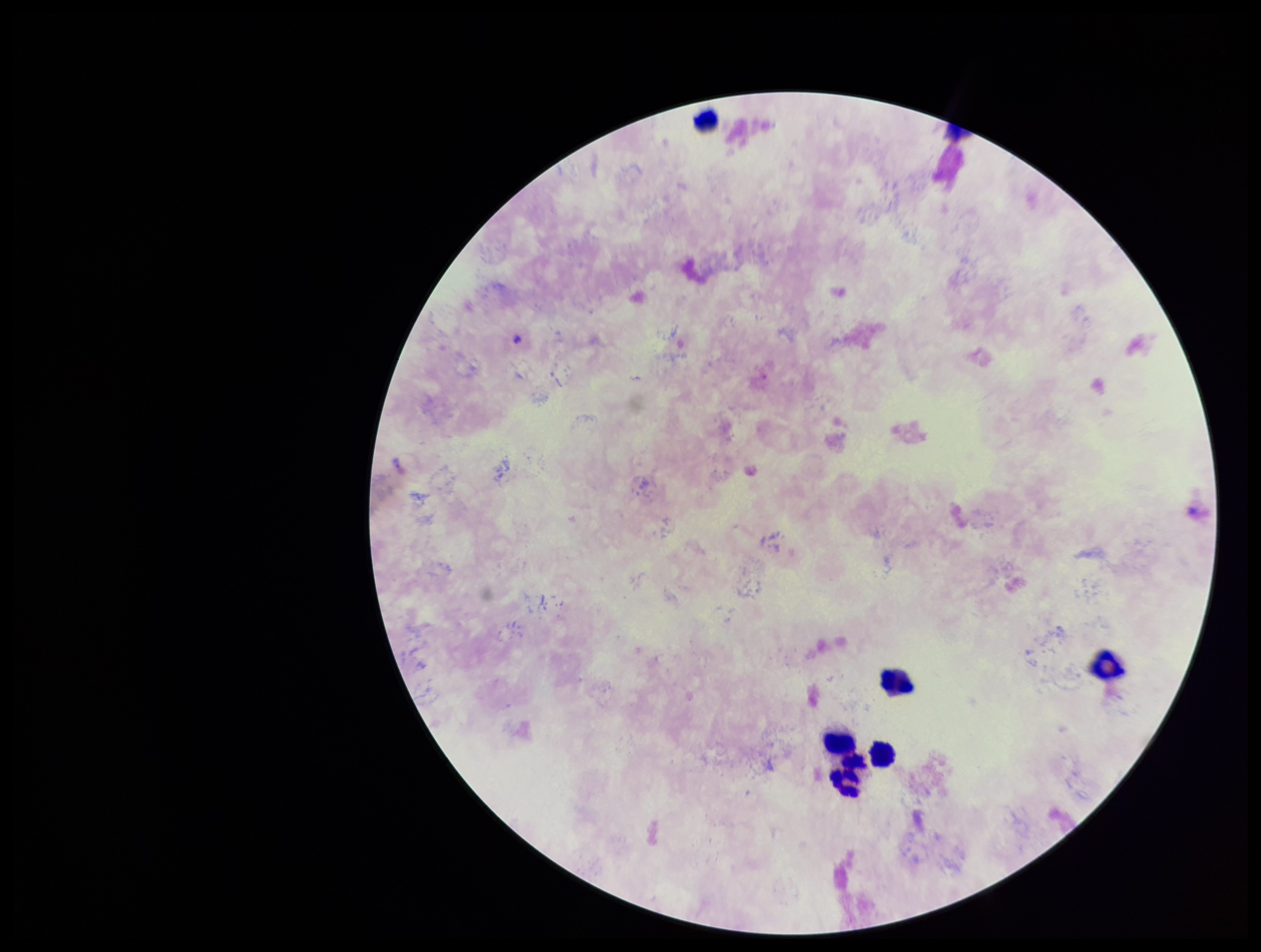
Leukocyte count: 6. Image is 1261×952 pixels. Species reported for this patient: Plasmodium falciparum. Plasmodium parasites: none seen. One field from this slide. Stained with Giemsa. Smartphone photograph taken through the eyepiece of a microscope. Parasite count: 0. Preparation: thick blood smear. Patient malaria status: positive.